Report the malaria status of this cell.
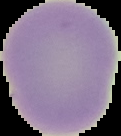
It is uninfected.

From a thin blood film. Image is 121×136 pixels. Cell region segmented out of the field of view; the surrounding area is masked to black.